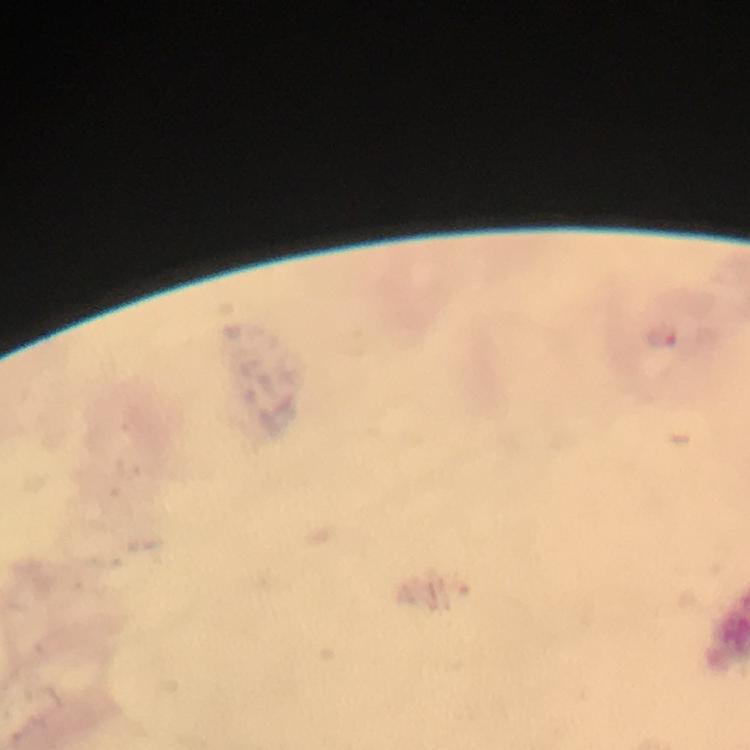
Approximate object centers, in pixels from the top-left corner.
Summary:
  - Malaria parasite locations: (x=660, y=336)
  - Preparation: thick blood film
  - Capture: smartphone camera through the microscope
  - Stain: Giemsa
  - Magnification: 100x
  - Immersion oil: used
  - Cropped from: a single field of view
  - Image size: 750×750 pixels
  - Context: from a malaria diagnostic workup